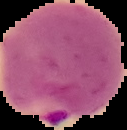
Result: malaria parasites detected. Image is 127×130 pixels. From a thin blood smear. Segmented cell region on a black background.